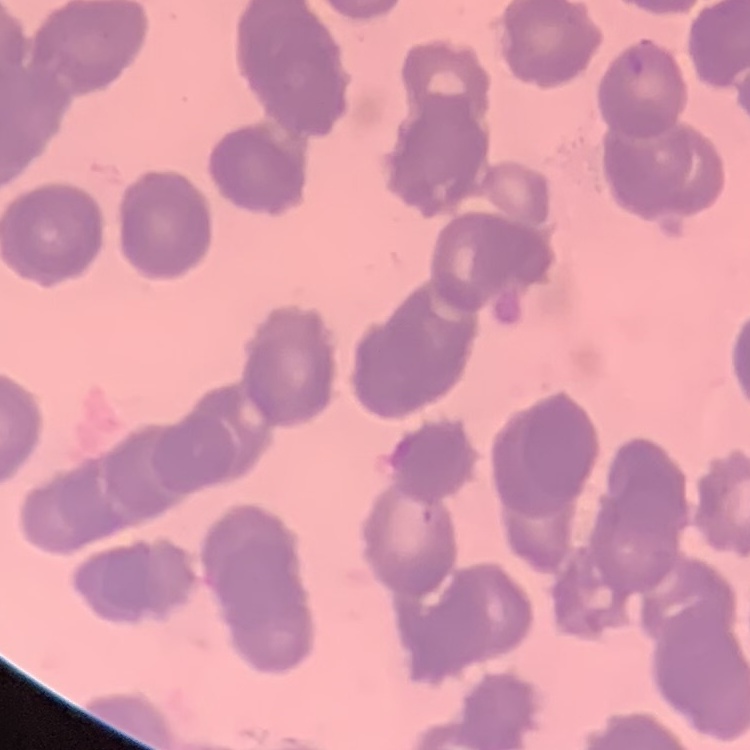
Summary:
  - Red blood cell morphology: rouleaux formation
  - Image type: square crop of a larger photomicrograph
  - Stain: Field's or Giemsa
  - Preparation: thin peripheral smear